Mark where leukocytes are.
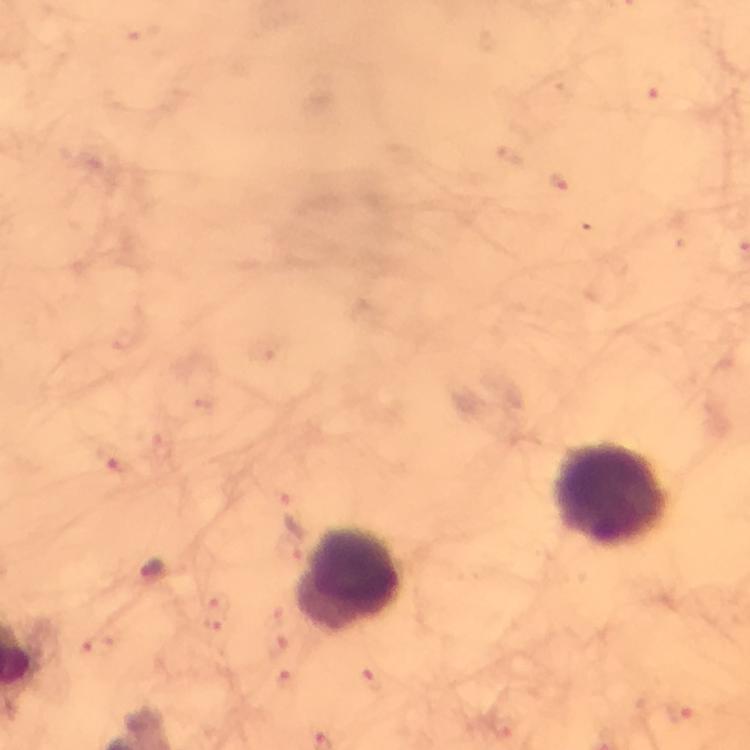

Approximate object centers, in pixels from the top-left corner.
Leukocytes: (x=611, y=494), (x=352, y=579).

Summary:
  - Plasmodium parasite locations: (x=650, y=88), (x=560, y=180), (x=112, y=458), (x=218, y=602), (x=212, y=624), (x=98, y=646), (x=372, y=679), (x=681, y=711)
  - Cropped from: one field of view
  - Image size: 750×750 pixels
  - Capture: smartphone camera through the microscope
  - Context: from a diagnostic examination for malaria
  - Stain: Giemsa
  - Preparation: thick smear
  - Magnification: 100x
  - Immersion oil: used